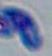
{
  "magnification": "1000x",
  "modality": "photomicrograph",
  "identification": "Toxoplasma gondii"
}